Report the malaria status of this cell.
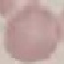

Uninfected.

Summary:
  - Stain: Giemsa
  - Capture: smartphone through the microscope eyepiece
  - Preparation: thin smear
  - Image type: cell patch, automatically extracted from a larger field of view and resized to 64 × 64 pixels